Point out each malaria parasite.
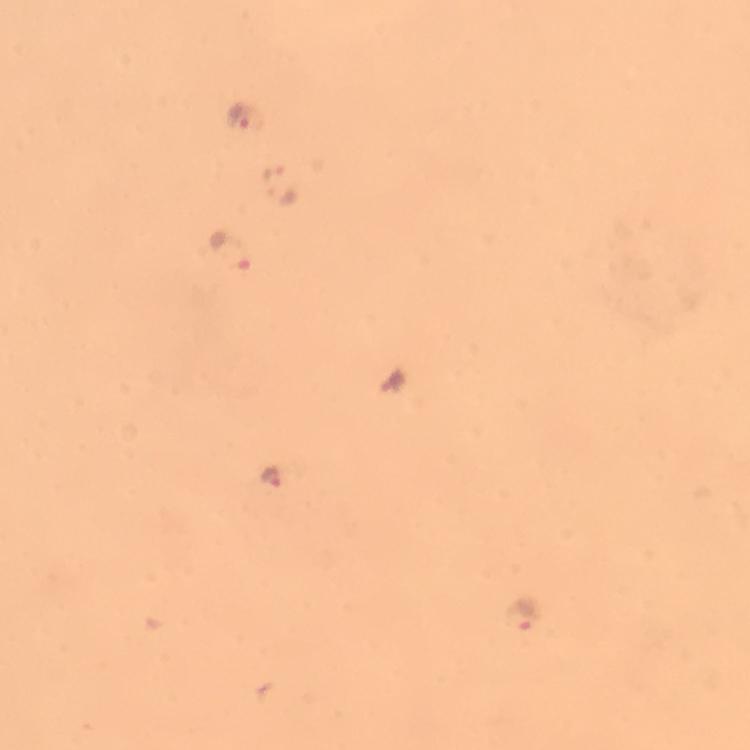
Approximate object centers, in pixels from the top-left corner.
Malaria parasites: (x=250, y=119), (x=230, y=249), (x=272, y=480), (x=518, y=617).

immersion_oil: applied
stain: Giemsa
context: from a malaria diagnostic workup
image_size: 750×750 pixels
magnification: 100x
capture: smartphone camera through the microscope
preparation: thick blood film
cropped_from: a single field of view